Assess this cell for malaria.
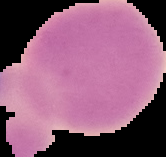
It is uninfected.

Summary:
  - Image size: 166×157 pixels
  - Preparation: thin blood film
  - Image type: segmented cell region with the area outside set to black